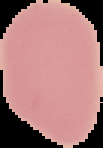
Summary:
  - Result: no malaria parasites detected
  - Preparation: thin blood smear
  - Image size: 103×148 pixels
  - Image type: segmented cell region with the area outside set to black